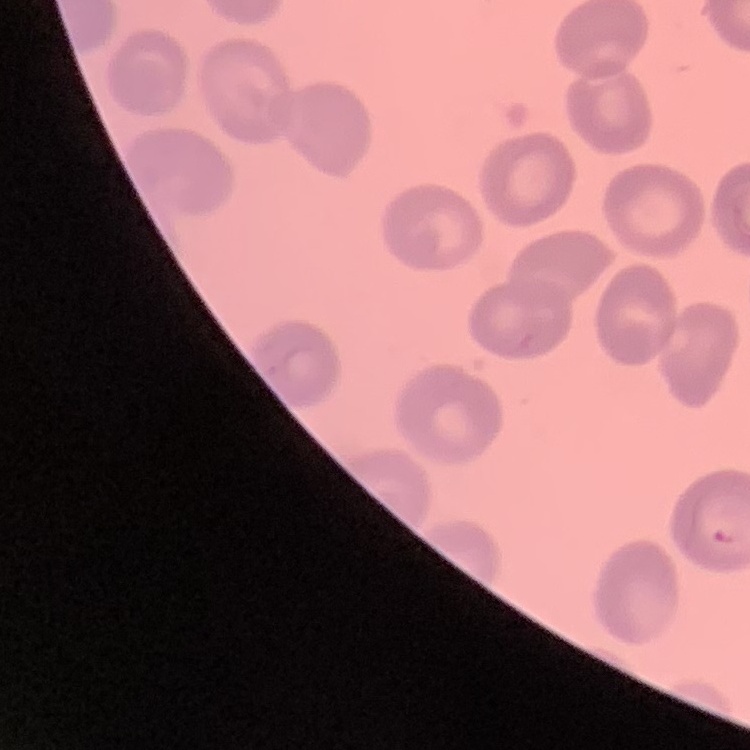

The red blood cells exhibit no rouleaux formation. Thin blood smear. One tile cut from a larger photomicrograph. Stained with either Field's or Giemsa.